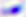

{
  "modality": "micrograph",
  "magnification": "400x",
  "identification": "Toxoplasma gondii"
}